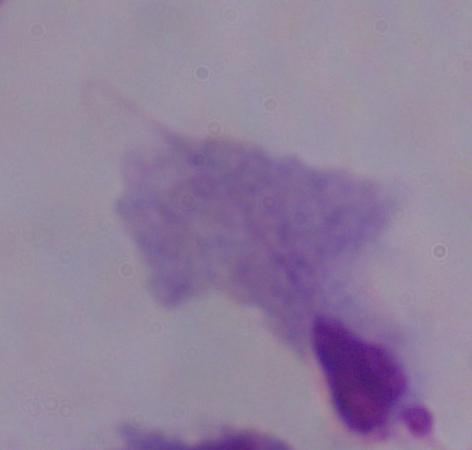
A trichomonad is shown. 1000x magnification. Photomicrograph.